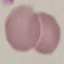
result: no malaria parasites seen
capture: smartphone camera at the microscope eyepiece
stain: Giemsa
preparation: thin blood film
image_type: cell patch, automatically extracted from a larger field of view and resized to 64 × 64 pixels